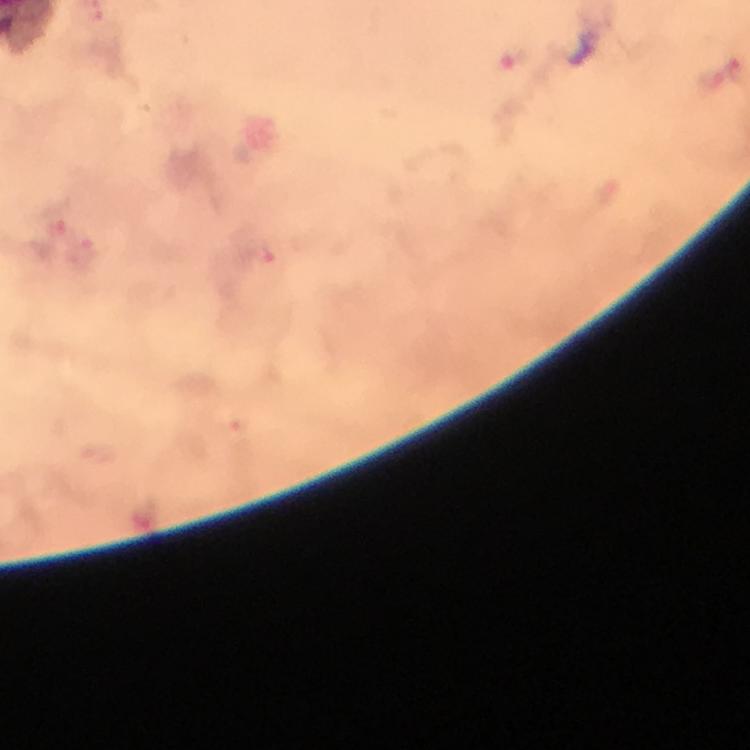
image size = 750×750 pixels
preparation = thick blood smear
magnification = 100x
cropped from = one field of view
Plasmodium parasite locations = approximate centers as {x, y} in pixels: {708, 78}, {53, 216}, {82, 251}, {260, 255}
capture = smartphone photograph through a microscope
stain = Giemsa
immersion oil = used
context = from a malaria diagnostic workup